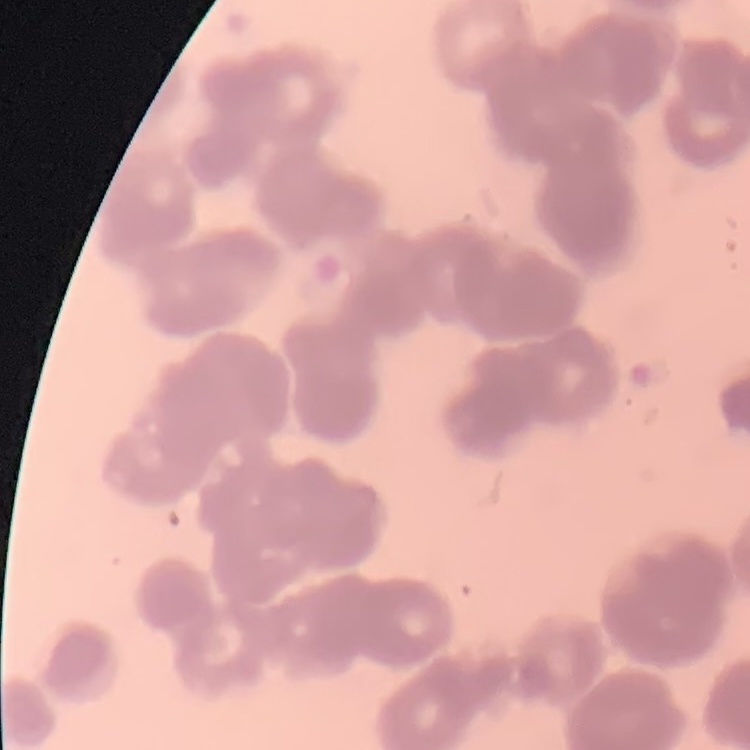
The erythrocytes exhibit rouleaux formation. Thin peripheral smear. Field's or Giemsa stain. One tile cut from a larger photomicrograph.